Report the malaria status of this cell.
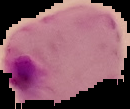
Parasitized.

From a thin blood smear. The area outside the segmented cell region is set to black. Image is 130×109 pixels.